Classify this cell by malaria status.
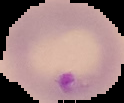

Parasitized.

Cell region segmented out of the field of view; the surrounding area is masked to black. From a thin blood smear. Image is 124×103 pixels.